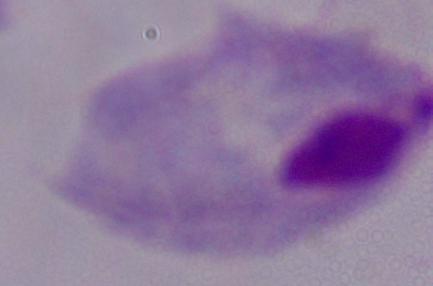

Summary:
  - Magnification: 1000x
  - Identification: trichomonad
  - Modality: photomicrograph